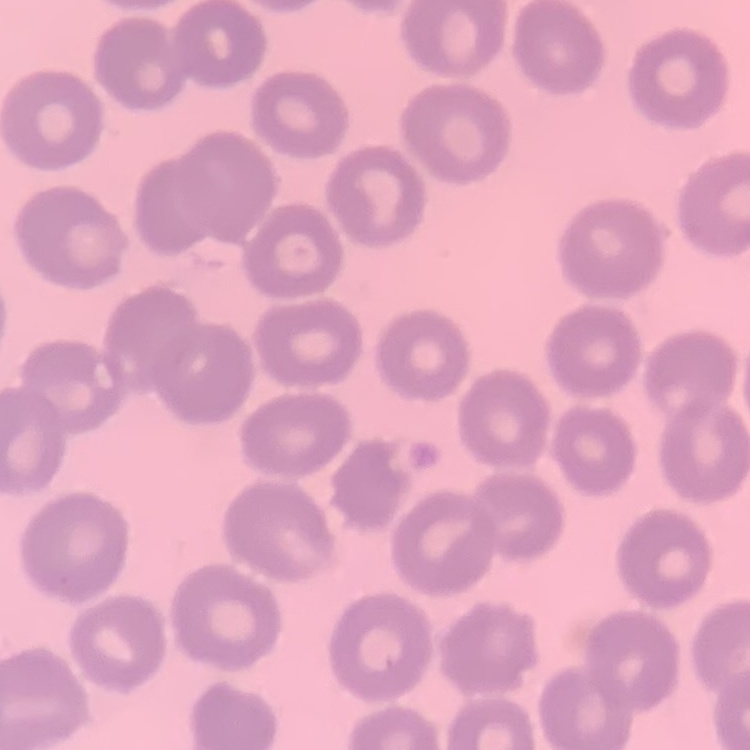 The erythrocytes exhibit no rouleaux formation. Thin blood smear. One tile cut from a larger photomicrograph. Field's or Giemsa stain.